Assess this cell for malaria.
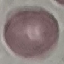

Uninfected.

Automatically extracted cell patch, resized to 64 × 64 pixels. Giemsa-stained preparation. Photographed with a smartphone camera at the microscope eyepiece. Thin blood film.